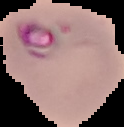

Summary:
  - Image type: segmented cell region on a black background
  - Malaria status: parasitized
  - Preparation: thin blood film
  - Image size: 124×127 pixels